Classify this cell by malaria status.
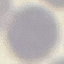

Uninfected.

Photographed with a smartphone camera at the microscope eyepiece. Automatically extracted cell patch, resized to 64 × 64 pixels. Thin blood smear. Giemsa-stained preparation.